State which parasite is depicted.
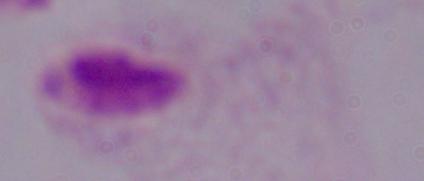

This is a trichomonad.

Summary:
  - Modality: micrograph
  - Magnification: 1000x